Outline each blood parasite and name the species.
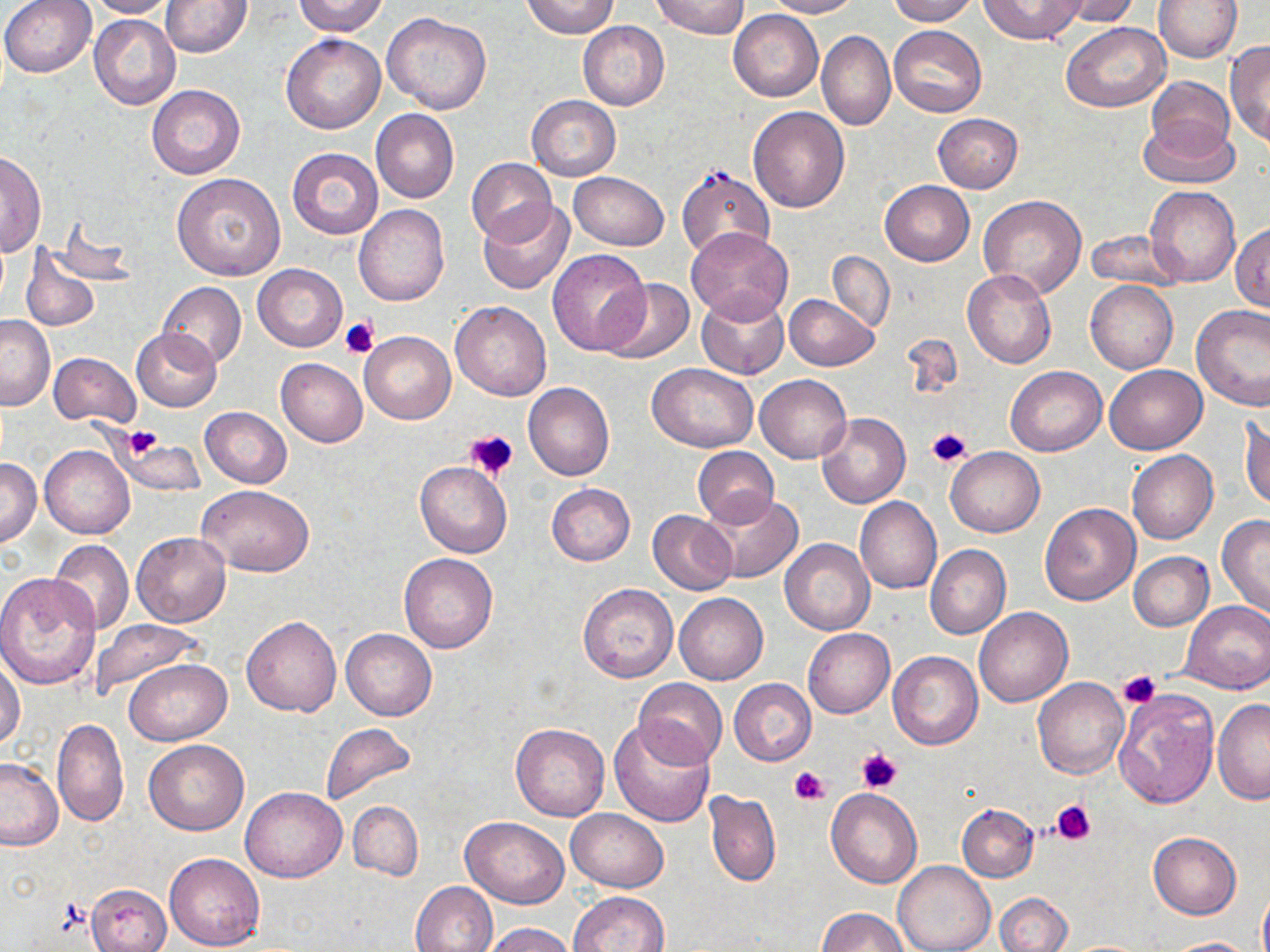

No blood parasites seen.

Approximate bounding boxes as [x1, y1, x2, y2] in pixels. Uninfected red blood cell locations: [0, 0, 99, 77], [86, 0, 178, 18], [161, 0, 253, 57], [293, 0, 387, 36], [522, 0, 618, 39], [652, 0, 748, 38], [765, 0, 862, 18], [885, 0, 977, 25], [977, 0, 1088, 44], [1049, 0, 1140, 27], [1152, 0, 1242, 62], [1, 7, 177, 93], [728, 10, 823, 101], [89, 12, 181, 109], [381, 12, 491, 113], [578, 21, 669, 110], [1061, 21, 1171, 112], [889, 25, 986, 117], [816, 31, 894, 130], [281, 33, 385, 134], [1225, 40, 1270, 149], [1146, 76, 1236, 156], [146, 83, 246, 179], [527, 95, 621, 180], [748, 106, 850, 213], [371, 109, 459, 202], [932, 114, 1024, 192], [1138, 116, 1238, 189], [287, 147, 383, 238], [0, 151, 44, 256], [466, 157, 557, 246], [674, 165, 776, 263], [568, 172, 670, 250], [172, 174, 286, 281], [878, 181, 975, 266], [1146, 185, 1240, 287], [979, 195, 1087, 300], [479, 200, 574, 295], [354, 204, 450, 308], [47, 217, 138, 287], [1231, 223, 1269, 312], [685, 227, 793, 323], [1084, 231, 1187, 292], [22, 247, 100, 333], [547, 248, 650, 356], [827, 251, 894, 330], [252, 264, 347, 351], [962, 269, 1057, 370], [600, 277, 694, 364], [1086, 280, 1177, 374], [158, 282, 246, 370], [697, 291, 789, 378], [784, 294, 878, 371], [451, 301, 552, 401], [1191, 305, 1270, 410], [0, 314, 54, 409], [132, 329, 223, 411], [359, 331, 456, 424], [900, 332, 964, 404], [49, 351, 141, 428], [276, 358, 367, 447], [648, 362, 759, 453], [1104, 364, 1206, 454], [1005, 366, 1107, 455], [754, 374, 851, 463], [523, 383, 614, 480], [200, 406, 292, 488], [1241, 411, 1269, 511], [817, 412, 910, 508], [115, 432, 202, 497], [40, 444, 135, 539], [692, 445, 778, 527], [945, 447, 1044, 537], [1127, 450, 1219, 544], [0, 457, 42, 548], [415, 462, 511, 557], [547, 483, 635, 565], [198, 484, 315, 577], [703, 491, 802, 584], [855, 496, 942, 594], [1038, 502, 1141, 605], [648, 509, 737, 595], [1217, 515, 1270, 619], [132, 532, 231, 628], [780, 538, 875, 635], [50, 540, 135, 635], [925, 544, 1012, 639], [1129, 552, 1214, 631], [399, 553, 498, 652], [0, 573, 102, 691], [578, 582, 679, 682], [675, 592, 768, 685], [1181, 599, 1270, 693], [974, 607, 1072, 707], [242, 614, 341, 716], [90, 618, 206, 699], [339, 627, 437, 721], [803, 627, 894, 718], [888, 651, 983, 750], [0, 658, 25, 750], [124, 658, 232, 745], [631, 677, 727, 769], [730, 678, 816, 764], [1032, 678, 1129, 779], [1113, 687, 1221, 810], [1213, 699, 1270, 804], [52, 717, 127, 827], [607, 719, 716, 827], [319, 722, 417, 807], [510, 723, 610, 821], [143, 739, 249, 835], [0, 756, 65, 851], [240, 786, 346, 882], [827, 788, 922, 888], [704, 791, 781, 887], [348, 800, 422, 881], [957, 804, 1038, 882], [567, 808, 668, 892], [460, 815, 569, 908], [1148, 831, 1241, 920], [165, 852, 265, 951], [894, 861, 995, 952], [411, 881, 498, 952], [86, 882, 171, 952], [1258, 886, 1270, 952], [570, 891, 670, 952], [995, 892, 1073, 952], [817, 908, 907, 952], [483, 923, 576, 952], [1164, 937, 1259, 952]. Platelet locations: [341, 317, 379, 358], [123, 426, 163, 457], [926, 427, 971, 469], [467, 429, 518, 479], [1119, 670, 1160, 707], [856, 748, 903, 793], [789, 767, 830, 805], [1051, 799, 1097, 846]. Slide-level diagnosis: no evidence of blood parasites. Image is 1270×952 pixels. Thin blood smear. Captured at 1000x magnification. Light microscopy. One field of a larger specimen. May-Grünwald-Giemsa stain.